Draw a bounding box around every leukocyte (white blood cell).
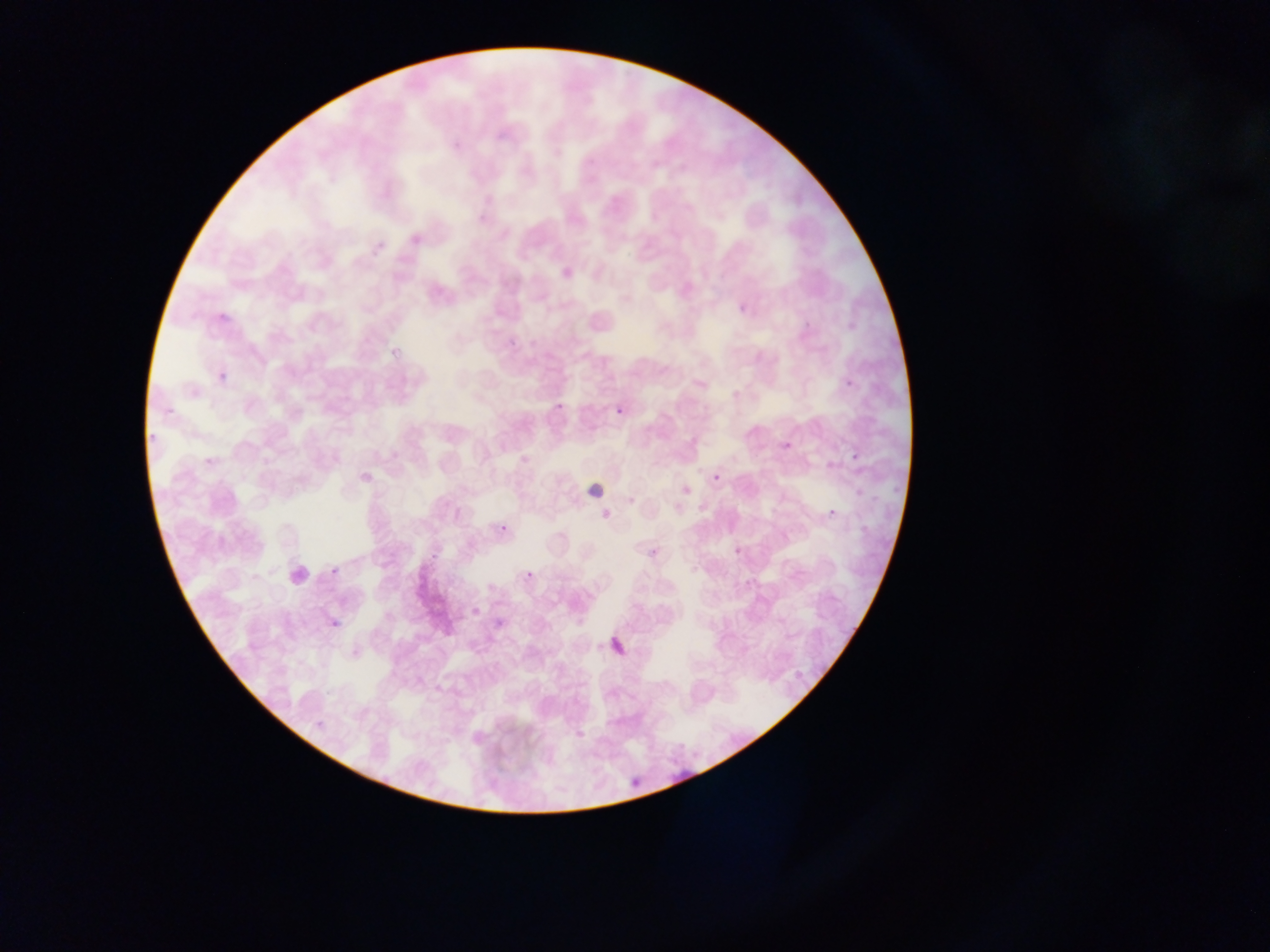
Approximate bounding boxes as (left, top, right, bottom) in pixels.
Leukocytes: (580, 460, 629, 505), (283, 549, 322, 589).

Summary:
  - Plasmodium parasite locations: (365, 235, 386, 255), (728, 303, 747, 317), (503, 323, 515, 347), (212, 361, 235, 381), (838, 377, 852, 394), (610, 384, 632, 420), (163, 398, 182, 413), (553, 403, 564, 418), (144, 430, 161, 446), (771, 434, 793, 452), (848, 447, 862, 461), (713, 475, 720, 483), (823, 505, 843, 527), (496, 513, 513, 543), (644, 535, 670, 560), (327, 562, 341, 581), (524, 571, 533, 580), (326, 608, 344, 634), (491, 613, 512, 637), (612, 622, 631, 666), (630, 760, 641, 791), (669, 770, 695, 785)
  - Country: Ghana
  - Image size: 1270×952 pixels
  - Preparation: thin blood smear
  - Capture: mobile-phone photograph through a microscope
  - Field of view: single